Comment on the morphology of the red blood cells.
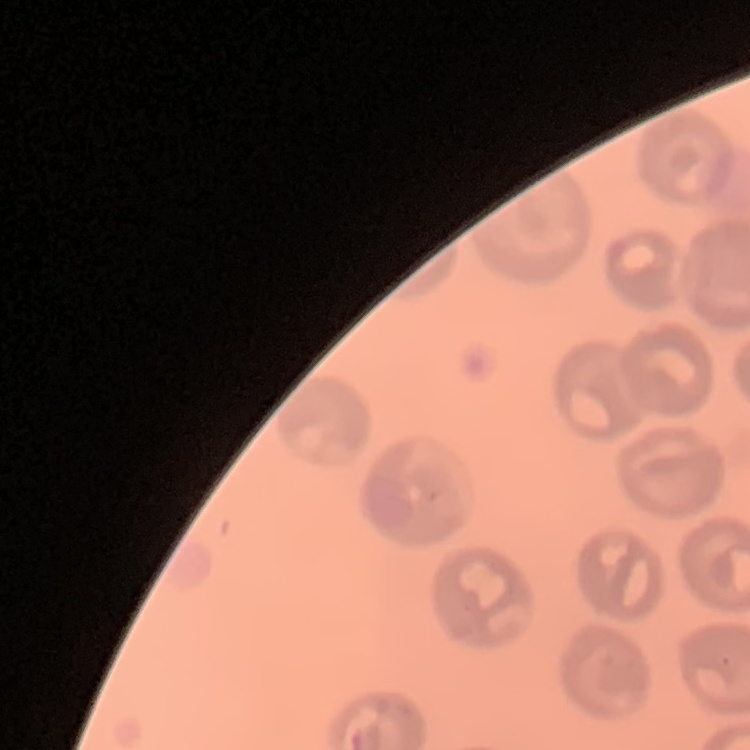
No rouleaux formation.

preparation = thin blood smear
stain = Field's or Giemsa
image type = square crop of a larger photomicrograph